Locate every malaria parasite.
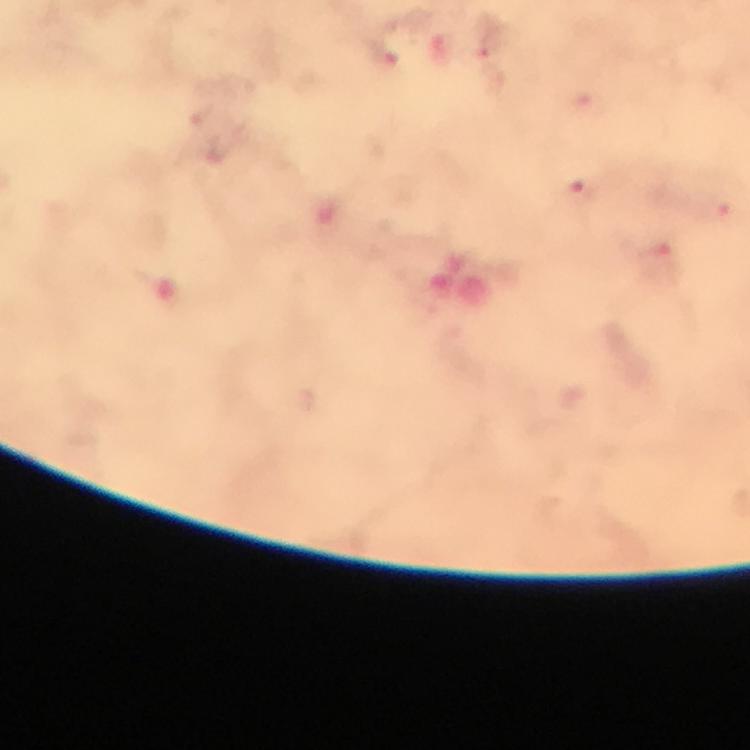
Approximate centers as {x, y} in pixels.
Malaria parasites: {488, 38}, {384, 59}, {579, 194}, {719, 209}.

cropped from = a single field of view
preparation = thick smear
immersion oil = applied
magnification = 100x
capture = smartphone photograph through a microscope
stain = Giemsa
context = from a malaria diagnostic workup
image size = 750×750 pixels